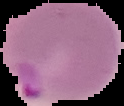

Image is 124×106 pixels. The area outside the segmented cell region is set to black. From a thin blood film. Result: Plasmodium parasites detected.